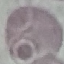
Summary:
  - Malaria status: uninfected
  - Image type: automatically extracted cell patch, resized to 64 × 64 pixels
  - Stain: Giemsa
  - Capture: smartphone camera at the microscope eyepiece
  - Preparation: thin blood smear